Identify the parasite.
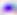

Toxoplasma gondii.

Micrograph. Captured at 400x magnification.